Classify this cell by malaria status.
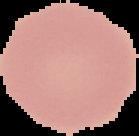

It is uninfected.

image size = 139×136 pixels
preparation = thin blood film
image type = segmented cell region with the area outside set to black